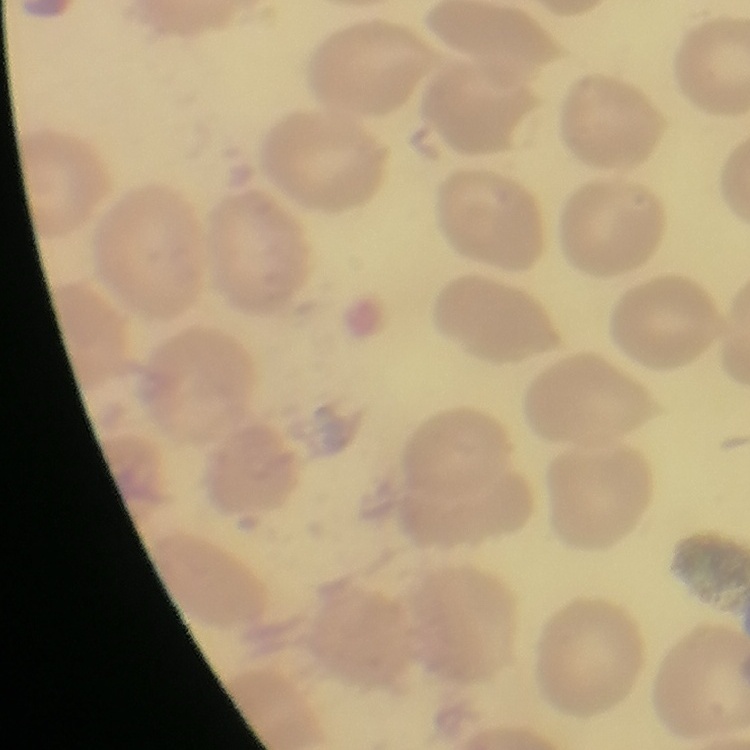
red blood cell morphology = no rouleaux formation
image type = square crop of a larger photomicrograph
stain = Field's or Giemsa
preparation = thin blood film